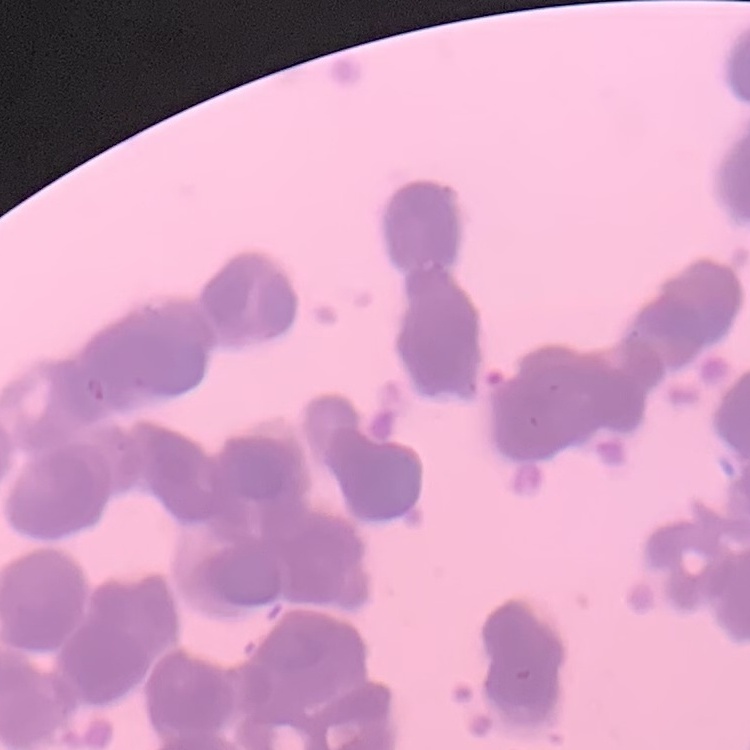
Summary:
  - Erythrocyte morphology: rouleaux formation
  - Preparation: thin peripheral smear
  - Stain: Field's or Giemsa
  - Image type: square crop of a larger photomicrograph